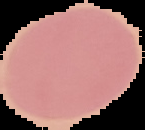
{
  "preparation": "thin blood film",
  "result": "no Plasmodium parasites detected",
  "image_size": "145×130 pixels",
  "image_type": "segmented cell region with the area outside set to black"
}